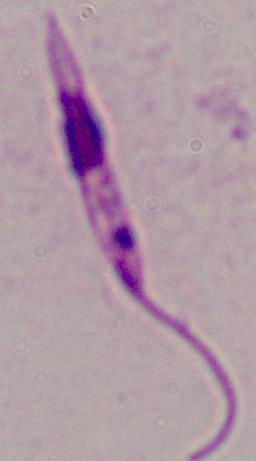
magnification: 1000x
modality: photomicrograph
identification: Leishmania